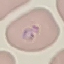 Result: malaria parasites detected. Automatically extracted cell patch, resized to 64 × 64 pixels. Acquired by smartphone through the microscope eyepiece. Thin smear of blood. Giemsa stain.